Locate every uninfected red blood cell.
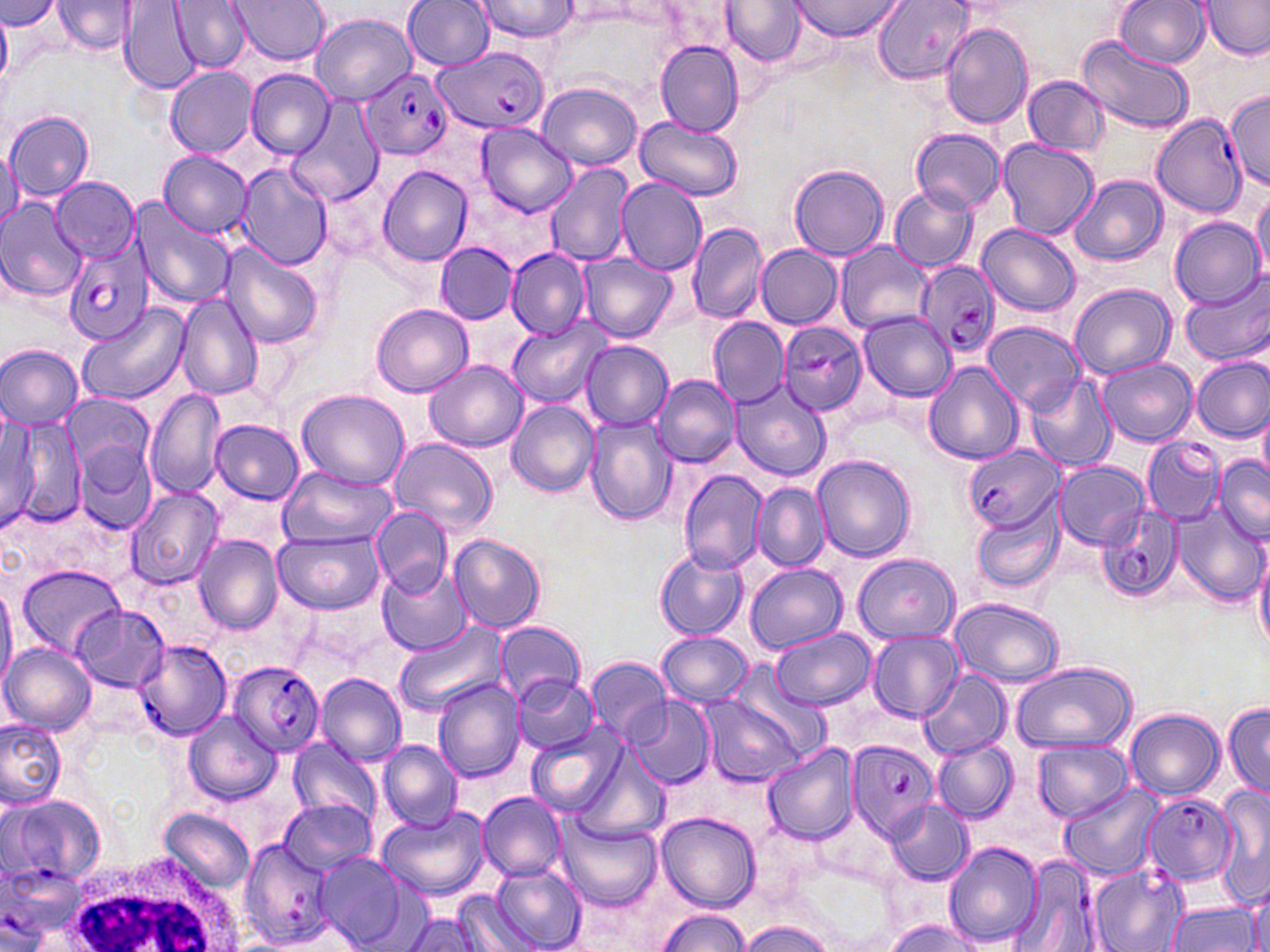

Approximate bounding boxes as named x1/y1/x2/y2 corners in pixels.
Uninfected red blood cells: (x1=0, y1=0, x2=60, y2=32), (x1=228, y1=0, x2=330, y2=64), (x1=473, y1=0, x2=578, y2=42), (x1=787, y1=0, x2=904, y2=42), (x1=1113, y1=0, x2=1210, y2=67), (x1=1199, y1=0, x2=1269, y2=61), (x1=171, y1=1, x2=250, y2=71), (x1=401, y1=1, x2=496, y2=72), (x1=874, y1=1, x2=976, y2=83), (x1=54, y1=2, x2=138, y2=55), (x1=120, y1=2, x2=200, y2=93), (x1=557, y1=2, x2=649, y2=23), (x1=721, y1=2, x2=804, y2=67), (x1=309, y1=13, x2=417, y2=104), (x1=940, y1=23, x2=1034, y2=127), (x1=1077, y1=34, x2=1195, y2=133), (x1=655, y1=40, x2=744, y2=137), (x1=166, y1=67, x2=257, y2=157), (x1=247, y1=70, x2=335, y2=159), (x1=1023, y1=77, x2=1110, y2=156), (x1=537, y1=81, x2=641, y2=170), (x1=1226, y1=90, x2=1270, y2=191), (x1=288, y1=93, x2=385, y2=205), (x1=6, y1=110, x2=96, y2=200), (x1=634, y1=115, x2=745, y2=200), (x1=475, y1=121, x2=577, y2=217), (x1=910, y1=128, x2=1009, y2=214), (x1=996, y1=140, x2=1098, y2=239), (x1=0, y1=147, x2=23, y2=231), (x1=157, y1=150, x2=253, y2=237), (x1=237, y1=163, x2=332, y2=268), (x1=544, y1=164, x2=635, y2=265), (x1=787, y1=164, x2=889, y2=262), (x1=377, y1=166, x2=473, y2=265), (x1=1070, y1=175, x2=1167, y2=265), (x1=51, y1=177, x2=139, y2=261), (x1=616, y1=178, x2=706, y2=276), (x1=889, y1=185, x2=978, y2=271), (x1=644, y1=189, x2=762, y2=312), (x1=1251, y1=191, x2=1270, y2=282), (x1=0, y1=199, x2=87, y2=302), (x1=131, y1=201, x2=233, y2=309), (x1=1169, y1=217, x2=1265, y2=310), (x1=686, y1=222, x2=767, y2=324), (x1=977, y1=223, x2=1080, y2=315), (x1=219, y1=240, x2=323, y2=349), (x1=836, y1=240, x2=934, y2=335), (x1=434, y1=242, x2=519, y2=324), (x1=756, y1=245, x2=843, y2=327), (x1=506, y1=248, x2=591, y2=338), (x1=579, y1=252, x2=677, y2=342), (x1=1181, y1=274, x2=1270, y2=368), (x1=1069, y1=283, x2=1176, y2=380), (x1=176, y1=293, x2=264, y2=400), (x1=77, y1=302, x2=189, y2=405), (x1=371, y1=303, x2=473, y2=397), (x1=859, y1=311, x2=956, y2=401), (x1=507, y1=317, x2=610, y2=409), (x1=709, y1=317, x2=789, y2=405), (x1=983, y1=321, x2=1083, y2=413), (x1=581, y1=342, x2=671, y2=429), (x1=0, y1=344, x2=84, y2=428), (x1=1097, y1=357, x2=1197, y2=447), (x1=1193, y1=357, x2=1269, y2=441), (x1=425, y1=359, x2=526, y2=452), (x1=923, y1=361, x2=1024, y2=465), (x1=652, y1=373, x2=740, y2=468), (x1=1024, y1=375, x2=1116, y2=473), (x1=731, y1=382, x2=831, y2=481), (x1=146, y1=388, x2=226, y2=499), (x1=297, y1=388, x2=409, y2=488), (x1=63, y1=392, x2=154, y2=477), (x1=507, y1=400, x2=602, y2=497), (x1=1257, y1=408, x2=1270, y2=486), (x1=2, y1=416, x2=86, y2=529), (x1=584, y1=416, x2=676, y2=524), (x1=211, y1=420, x2=303, y2=504), (x1=389, y1=438, x2=498, y2=535), (x1=76, y1=447, x2=157, y2=534), (x1=811, y1=455, x2=916, y2=562), (x1=1214, y1=457, x2=1270, y2=544), (x1=1054, y1=461, x2=1149, y2=548), (x1=277, y1=467, x2=395, y2=549), (x1=678, y1=469, x2=768, y2=574), (x1=751, y1=482, x2=829, y2=571), (x1=125, y1=487, x2=224, y2=590), (x1=1174, y1=500, x2=1265, y2=609), (x1=973, y1=507, x2=1065, y2=593), (x1=372, y1=508, x2=452, y2=594), (x1=273, y1=531, x2=385, y2=614), (x1=450, y1=534, x2=546, y2=632), (x1=194, y1=535, x2=283, y2=633), (x1=1252, y1=538, x2=1270, y2=655), (x1=654, y1=548, x2=749, y2=640), (x1=851, y1=553, x2=961, y2=644), (x1=377, y1=561, x2=471, y2=656), (x1=744, y1=563, x2=848, y2=655), (x1=17, y1=565, x2=128, y2=659), (x1=0, y1=580, x2=17, y2=696), (x1=950, y1=598, x2=1064, y2=686), (x1=71, y1=605, x2=172, y2=691), (x1=394, y1=620, x2=507, y2=722), (x1=493, y1=622, x2=586, y2=704), (x1=771, y1=629, x2=877, y2=710), (x1=656, y1=630, x2=753, y2=705), (x1=867, y1=631, x2=963, y2=722), (x1=1, y1=643, x2=98, y2=735), (x1=584, y1=656, x2=672, y2=742), (x1=1011, y1=662, x2=1136, y2=751), (x1=726, y1=664, x2=832, y2=761), (x1=916, y1=669, x2=1009, y2=761), (x1=315, y1=672, x2=407, y2=766), (x1=513, y1=675, x2=598, y2=753), (x1=432, y1=677, x2=527, y2=785), (x1=703, y1=696, x2=808, y2=786), (x1=627, y1=699, x2=716, y2=788), (x1=1222, y1=699, x2=1269, y2=801), (x1=181, y1=710, x2=282, y2=803), (x1=1123, y1=710, x2=1225, y2=801), (x1=0, y1=718, x2=68, y2=809), (x1=527, y1=727, x2=625, y2=816), (x1=288, y1=737, x2=381, y2=823), (x1=932, y1=738, x2=1019, y2=824), (x1=1032, y1=738, x2=1131, y2=823), (x1=378, y1=740, x2=463, y2=831), (x1=575, y1=744, x2=674, y2=845), (x1=761, y1=745, x2=860, y2=843), (x1=1058, y1=783, x2=1164, y2=879), (x1=1211, y1=787, x2=1270, y2=907), (x1=478, y1=792, x2=565, y2=881), (x1=279, y1=799, x2=377, y2=877), (x1=884, y1=800, x2=973, y2=884), (x1=377, y1=808, x2=490, y2=900), (x1=159, y1=809, x2=254, y2=893), (x1=657, y1=812, x2=760, y2=911), (x1=555, y1=816, x2=662, y2=911), (x1=943, y1=841, x2=1043, y2=948), (x1=313, y1=852, x2=406, y2=948), (x1=488, y1=864, x2=587, y2=952), (x1=1243, y1=878, x2=1270, y2=952), (x1=456, y1=893, x2=538, y2=951), (x1=1167, y1=900, x2=1262, y2=951), (x1=656, y1=909, x2=752, y2=951), (x1=403, y1=912, x2=482, y2=952), (x1=737, y1=919, x2=836, y2=952), (x1=882, y1=919, x2=984, y2=952).

Summary:
  - Plasmodium falciparum-infected red blood cell locations: (x1=434, y1=46, x2=548, y2=135), (x1=361, y1=67, x2=452, y2=161), (x1=1152, y1=113, x2=1245, y2=216), (x1=65, y1=239, x2=154, y2=346), (x1=915, y1=259, x2=1000, y2=361), (x1=777, y1=321, x2=867, y2=418), (x1=1142, y1=437, x2=1226, y2=523), (x1=963, y1=445, x2=1063, y2=534), (x1=1095, y1=507, x2=1186, y2=600), (x1=133, y1=640, x2=236, y2=742), (x1=229, y1=660, x2=326, y2=757), (x1=845, y1=737, x2=939, y2=841), (x1=3, y1=792, x2=106, y2=892), (x1=1141, y1=794, x2=1237, y2=888), (x1=239, y1=841, x2=335, y2=952), (x1=1010, y1=857, x2=1108, y2=952), (x1=1089, y1=864, x2=1189, y2=952)
  - White blood cell locations: (x1=63, y1=851, x2=237, y2=952)
  - Slide-level diagnosis: Plasmodium falciparum
  - Stain: May-Grünwald-Giemsa
  - Image size: 1270×952 pixels
  - Field of view: one of a larger specimen
  - Modality: optical microscopy
  - Magnification: 1000x
  - Preparation: thin blood film